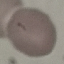

Malaria status: uninfected. Cell patch, automatically extracted from a larger field of view and resized to 64 × 64 pixels. Giemsa-stained preparation. Thin blood smear. Photographed with a smartphone camera at the microscope eyepiece.